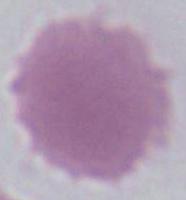
An erythrocyte is shown. Photomicrograph. 1000x magnification.